Locate every Plasmodium parasite.
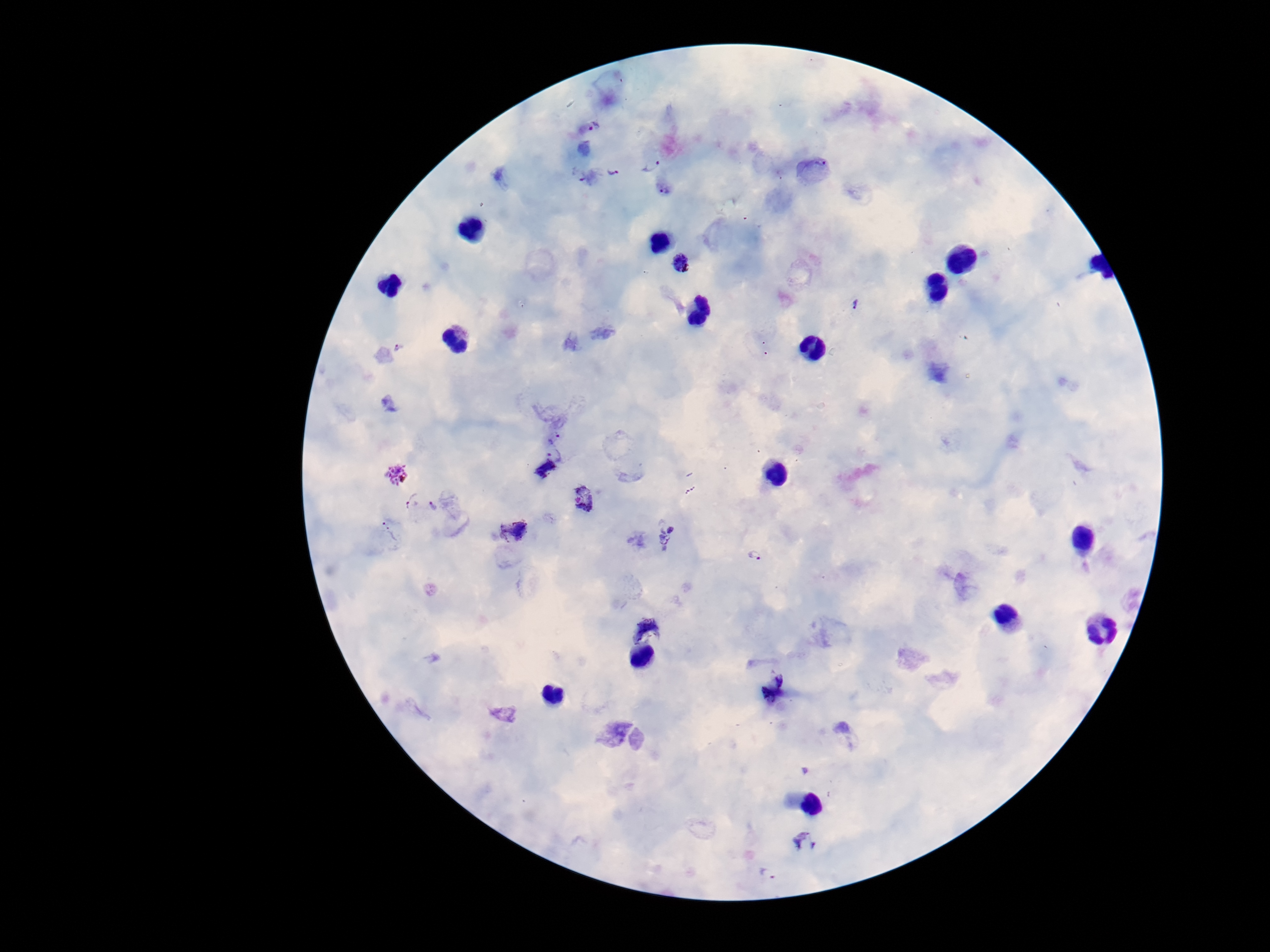

Approximate centers as (x, y) in pixels.
Plasmodium parasites: (592, 128), (649, 162), (612, 169), (815, 170), (578, 174), (666, 188), (681, 264), (855, 305), (399, 347), (553, 436), (555, 455), (543, 468), (397, 475), (586, 497), (411, 502), (434, 506), (388, 531), (514, 531), (672, 536), (754, 555), (646, 629), (772, 689), (845, 736), (805, 842), (769, 874).

image_size: 1270×952 pixels
field_of_view: one from this slide
capture: smartphone camera through the microscope eyepiece
magnification: 100x
patient_malaria_status: positive
stain: Giemsa
preparation: thick blood film